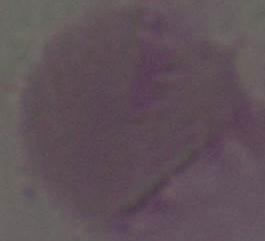

magnification: 1000x
identification: red blood cell
modality: photomicrograph